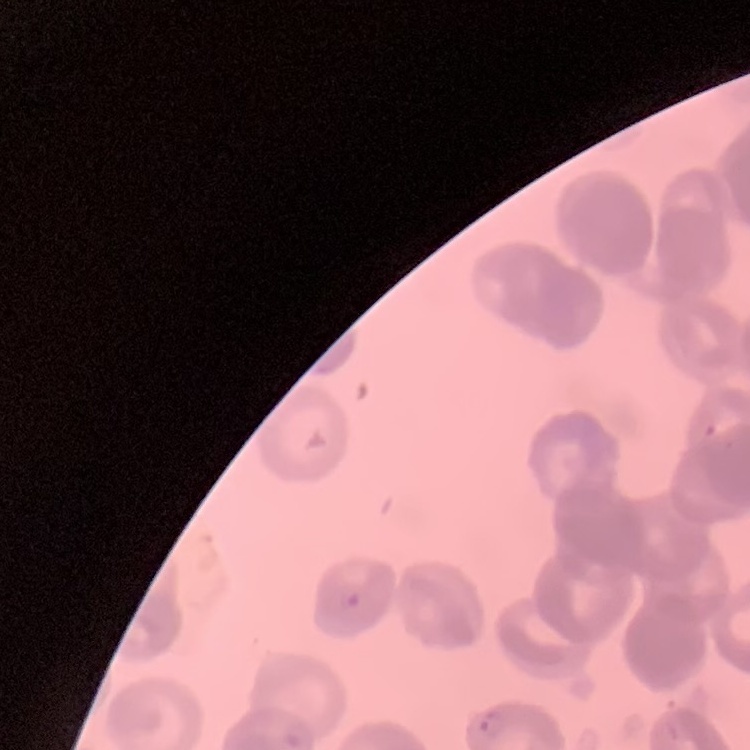
erythrocyte_morphology: rouleaux formation
image_type: one tile cut from a larger photomicrograph
preparation: thin blood film
stain: Field's or Giemsa